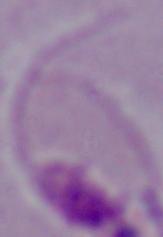

Summary:
  - Identification: Leishmania
  - Modality: photomicrograph
  - Magnification: 1000x